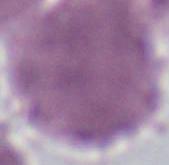
Summary:
  - Modality: micrograph
  - Identification: erythrocyte
  - Magnification: 1000x